Assess the morphology of the red blood cells.
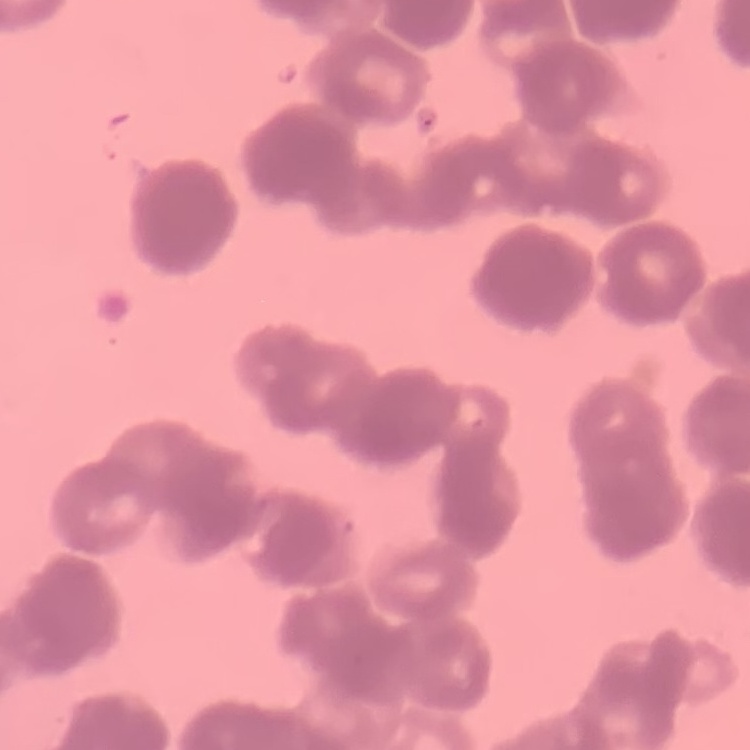

They show rouleaux formation.

Summary:
  - Image type: square crop of a larger photomicrograph
  - Preparation: thin peripheral smear
  - Stain: Field's or Giemsa